Name the cell type shown.
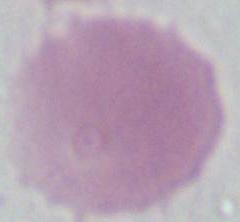

An erythrocyte.

Photomicrograph. Captured at 1000x magnification.